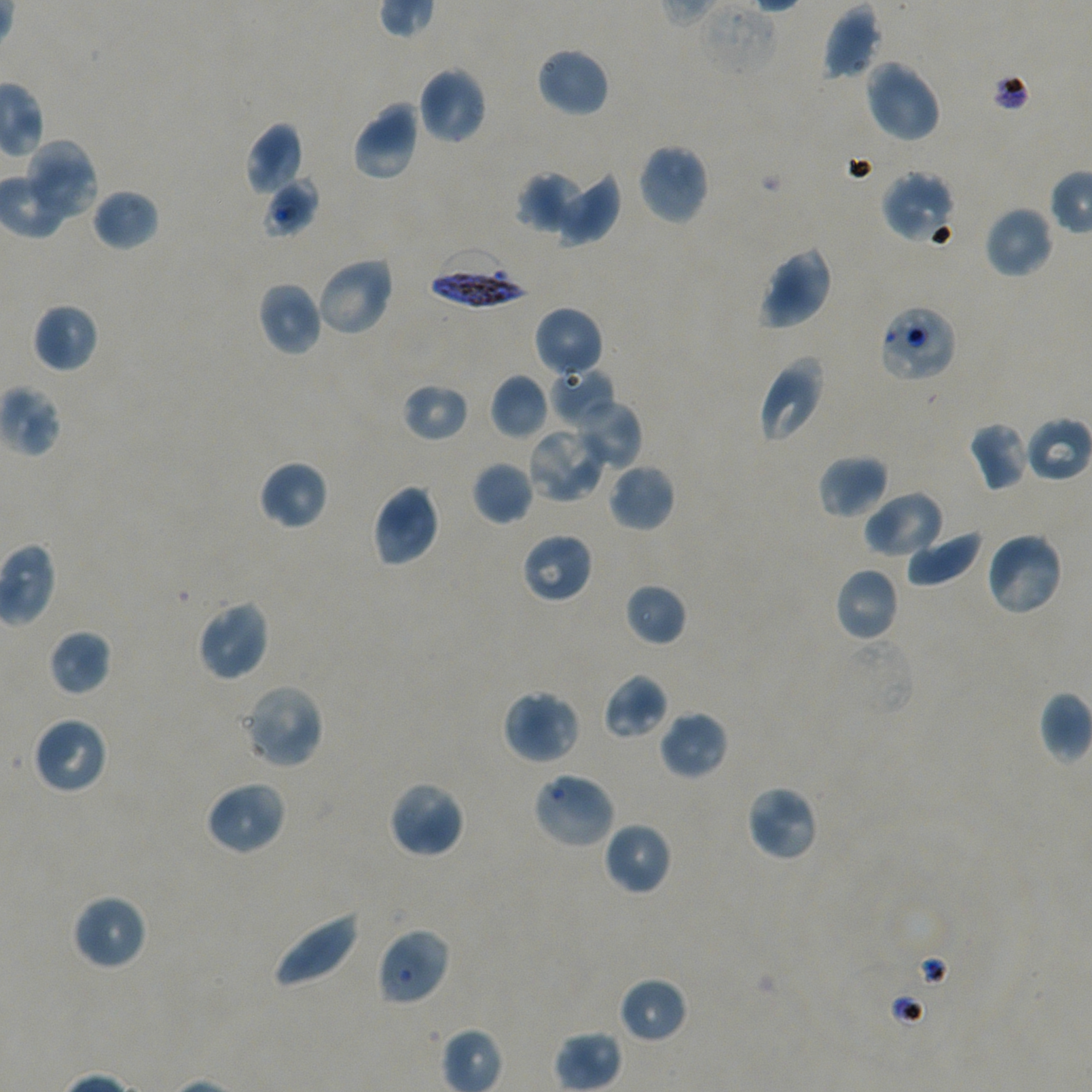

Approximate bounding boxes as [x1, y1, x2, y2] in pixels. Not every red blood cell is marked.
Summary:
  - Locations of uninfected red blood cells: [821, 4, 881, 80], [534, 46, 611, 118], [863, 58, 942, 143], [416, 65, 489, 145], [351, 100, 421, 182], [247, 123, 304, 196], [24, 139, 99, 222], [636, 142, 710, 227], [517, 170, 583, 234], [553, 170, 621, 246], [879, 170, 957, 244], [263, 177, 318, 238], [92, 188, 159, 251], [983, 205, 1055, 280], [757, 245, 833, 330], [314, 255, 395, 338], [257, 281, 323, 357], [32, 303, 99, 373], [532, 306, 604, 380], [757, 356, 827, 445], [490, 374, 549, 439], [401, 382, 469, 442], [570, 398, 643, 470], [967, 421, 1032, 492], [526, 426, 606, 505], [817, 454, 890, 520], [258, 459, 329, 531], [471, 460, 534, 526], [608, 462, 676, 533], [370, 483, 441, 568], [861, 490, 945, 560], [905, 529, 983, 587], [984, 530, 1065, 617], [520, 532, 594, 604], [833, 566, 900, 643], [624, 583, 687, 647], [196, 599, 270, 682], [48, 629, 111, 695], [602, 673, 669, 740], [242, 683, 325, 769], [502, 689, 581, 765], [1039, 691, 1092, 764], [657, 709, 729, 781], [31, 715, 109, 796], [531, 771, 618, 850], [204, 780, 288, 856], [388, 780, 466, 859], [745, 784, 820, 862], [602, 822, 672, 896], [71, 894, 147, 972], [270, 909, 361, 990], [376, 927, 452, 1006], [618, 976, 689, 1044], [555, 1030, 622, 1092]
  - Locations of red blood cells of indeterminate infection status: [702, 2, 779, 77], [877, 304, 958, 384], [548, 366, 617, 427], [1025, 416, 1092, 482]
  - Locations of infected red blood cells: [427, 248, 530, 310]
  - Image size: 1092×1092 pixels
  - Stain: Giemsa
  - Objective: 100x, oil immersion, numerical aperture 1.45
  - Donor blood group: A+/O+
  - Field of view: one from this slide
  - Culture: static in-vitro P. falciparum strain NF54
  - Preparation: thin blood smear